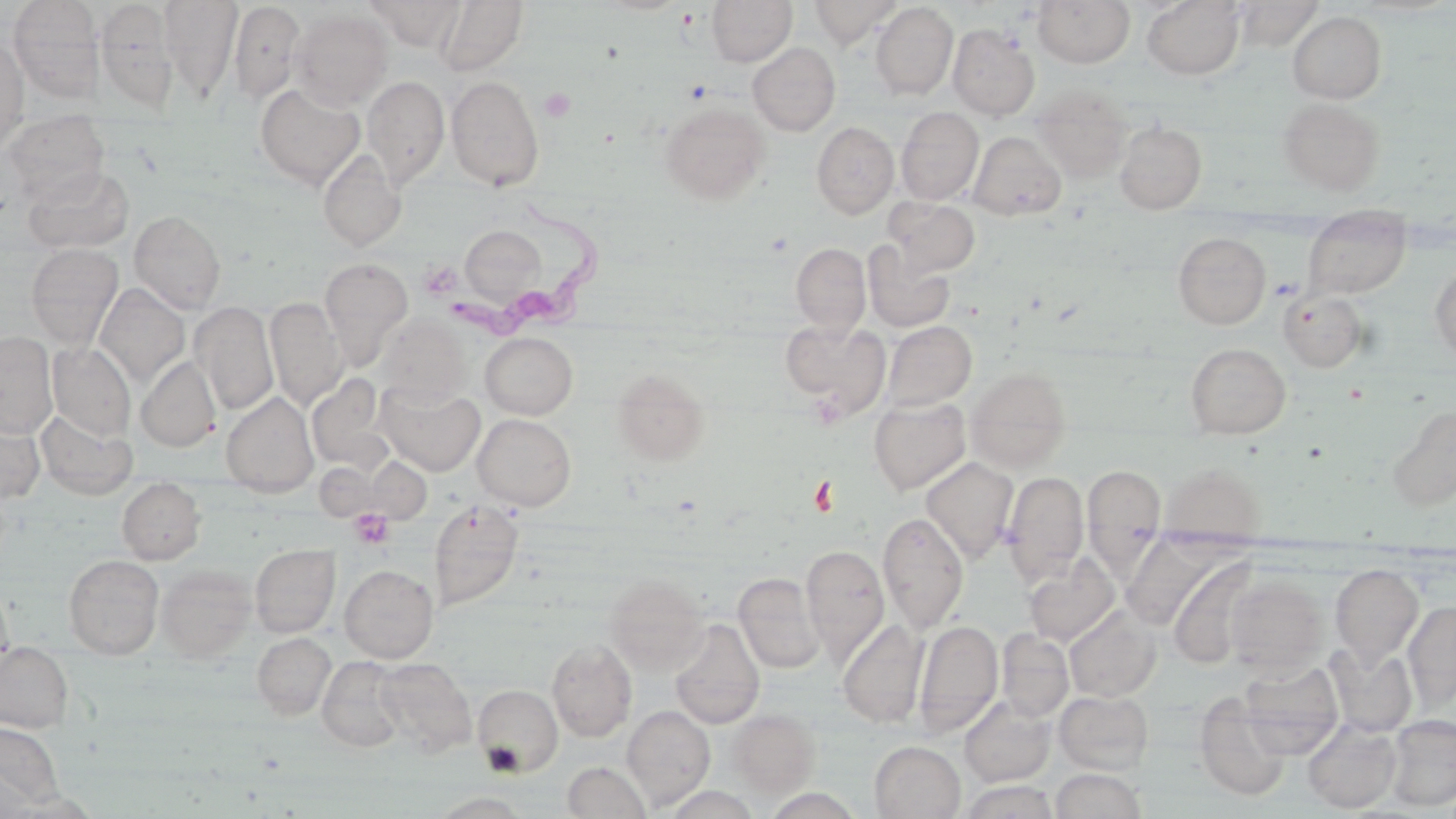
Approximate bounding boxes as named x1/y1/x2/y2 corners in pixels. Uninfected red blood cell locations: (x1=7, y1=0, x2=105, y2=102), (x1=93, y1=0, x2=179, y2=112), (x1=159, y1=0, x2=243, y2=100), (x1=366, y1=0, x2=465, y2=51), (x1=433, y1=0, x2=530, y2=76), (x1=707, y1=0, x2=797, y2=66), (x1=809, y1=0, x2=902, y2=48), (x1=1033, y1=0, x2=1135, y2=68), (x1=229, y1=1, x2=305, y2=105), (x1=1142, y1=1, x2=1246, y2=80), (x1=1235, y1=1, x2=1325, y2=49), (x1=870, y1=3, x2=958, y2=101), (x1=289, y1=9, x2=393, y2=110), (x1=1288, y1=11, x2=1386, y2=103), (x1=948, y1=24, x2=1040, y2=121), (x1=0, y1=37, x2=29, y2=154), (x1=748, y1=43, x2=841, y2=136), (x1=363, y1=74, x2=450, y2=191), (x1=446, y1=74, x2=545, y2=191), (x1=255, y1=83, x2=366, y2=190), (x1=1033, y1=85, x2=1132, y2=182), (x1=1278, y1=98, x2=1385, y2=194), (x1=659, y1=101, x2=770, y2=205), (x1=896, y1=107, x2=984, y2=204), (x1=2, y1=112, x2=109, y2=206), (x1=812, y1=121, x2=899, y2=218), (x1=1115, y1=121, x2=1207, y2=213), (x1=969, y1=132, x2=1067, y2=221), (x1=318, y1=148, x2=406, y2=252), (x1=24, y1=166, x2=134, y2=253), (x1=885, y1=197, x2=981, y2=277), (x1=129, y1=210, x2=226, y2=313), (x1=1303, y1=213, x2=1411, y2=299), (x1=460, y1=225, x2=546, y2=308), (x1=1173, y1=232, x2=1271, y2=329), (x1=862, y1=242, x2=956, y2=333), (x1=26, y1=243, x2=123, y2=348), (x1=791, y1=243, x2=871, y2=336), (x1=320, y1=257, x2=413, y2=371), (x1=1429, y1=263, x2=1456, y2=361), (x1=94, y1=283, x2=190, y2=387), (x1=1279, y1=289, x2=1367, y2=371), (x1=265, y1=297, x2=347, y2=410), (x1=190, y1=301, x2=279, y2=415), (x1=377, y1=315, x2=470, y2=403), (x1=780, y1=318, x2=890, y2=417), (x1=882, y1=321, x2=976, y2=411), (x1=0, y1=332, x2=57, y2=438), (x1=480, y1=332, x2=578, y2=419), (x1=47, y1=342, x2=136, y2=440), (x1=1185, y1=343, x2=1290, y2=439), (x1=136, y1=356, x2=221, y2=452), (x1=612, y1=368, x2=711, y2=465), (x1=966, y1=368, x2=1072, y2=471), (x1=305, y1=373, x2=388, y2=471), (x1=375, y1=382, x2=486, y2=476), (x1=221, y1=392, x2=319, y2=497), (x1=869, y1=397, x2=971, y2=495), (x1=1386, y1=404, x2=1456, y2=510), (x1=35, y1=410, x2=137, y2=500), (x1=0, y1=411, x2=45, y2=506), (x1=473, y1=414, x2=576, y2=511), (x1=921, y1=457, x2=1018, y2=561), (x1=1160, y1=461, x2=1267, y2=542), (x1=1083, y1=465, x2=1167, y2=558), (x1=1002, y1=471, x2=1089, y2=584), (x1=117, y1=477, x2=205, y2=564), (x1=429, y1=501, x2=524, y2=611), (x1=878, y1=512, x2=969, y2=633), (x1=1123, y1=536, x2=1217, y2=632), (x1=250, y1=544, x2=340, y2=637), (x1=801, y1=544, x2=889, y2=663), (x1=63, y1=554, x2=165, y2=659), (x1=1023, y1=555, x2=1120, y2=646), (x1=1168, y1=557, x2=1259, y2=669), (x1=1330, y1=563, x2=1424, y2=666), (x1=339, y1=564, x2=438, y2=663), (x1=155, y1=565, x2=256, y2=663), (x1=733, y1=572, x2=825, y2=673), (x1=603, y1=573, x2=709, y2=675), (x1=1224, y1=576, x2=1327, y2=674), (x1=0, y1=582, x2=13, y2=675), (x1=1403, y1=601, x2=1456, y2=711), (x1=1065, y1=607, x2=1160, y2=702), (x1=669, y1=619, x2=765, y2=730), (x1=838, y1=619, x2=929, y2=727), (x1=914, y1=619, x2=1003, y2=739), (x1=996, y1=628, x2=1074, y2=721), (x1=252, y1=632, x2=336, y2=719), (x1=547, y1=639, x2=637, y2=742), (x1=0, y1=641, x2=73, y2=731), (x1=1326, y1=645, x2=1417, y2=736), (x1=317, y1=656, x2=407, y2=752), (x1=375, y1=658, x2=476, y2=756), (x1=1239, y1=661, x2=1344, y2=757), (x1=473, y1=684, x2=563, y2=776), (x1=1054, y1=690, x2=1154, y2=775), (x1=1194, y1=693, x2=1291, y2=801), (x1=959, y1=696, x2=1057, y2=787), (x1=622, y1=705, x2=716, y2=810), (x1=727, y1=709, x2=821, y2=797), (x1=1385, y1=714, x2=1456, y2=811), (x1=1303, y1=720, x2=1402, y2=813), (x1=0, y1=723, x2=63, y2=809), (x1=870, y1=741, x2=965, y2=819), (x1=563, y1=761, x2=651, y2=819), (x1=1051, y1=769, x2=1146, y2=819), (x1=662, y1=786, x2=761, y2=819), (x1=763, y1=789, x2=864, y2=819), (x1=432, y1=792, x2=529, y2=818). Platelet locations: (x1=539, y1=88, x2=576, y2=122), (x1=349, y1=508, x2=395, y2=549). Trypanosoma brucei locations: (x1=449, y1=194, x2=601, y2=338). Slide-level diagnosis: Trypanosoma brucei. 1000x magnification. Thin blood smear. One field of a larger specimen. Light microscopy. May-Grünwald-Giemsa-stained preparation. Image is 1456×819 pixels.